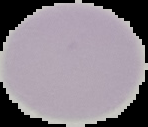
Summary:
  - Image size: 148×127 pixels
  - Image type: segmented cell region on a black background
  - Result: no malaria parasites seen
  - Preparation: thin blood smear